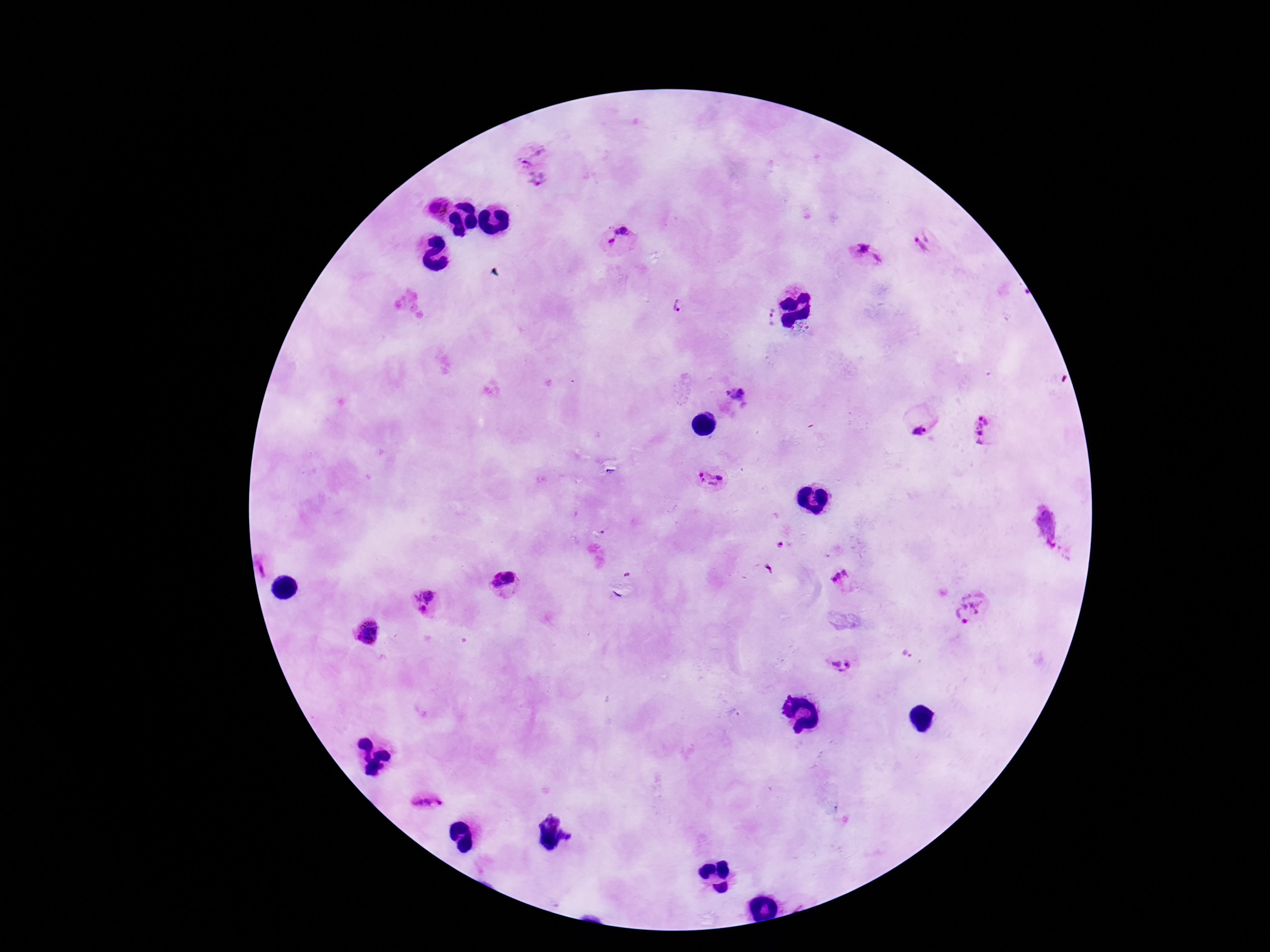
Approximate centers as [x, y] in pixels. Plasmodium parasite locations: [536, 166], [438, 210], [618, 238], [924, 243], [868, 255], [679, 305], [771, 317], [737, 395], [982, 432], [919, 434], [712, 479], [1047, 526], [780, 546], [260, 567], [841, 581], [505, 582], [423, 601], [970, 607], [369, 632], [838, 666], [425, 799]. Giemsa stain. Photographed through the microscope eyepiece with a smartphone camera. Patient malaria status: positive. Thick blood film. 100x magnification. Image is 1270×952 pixels. Single field of view.